Mark where platelets are.
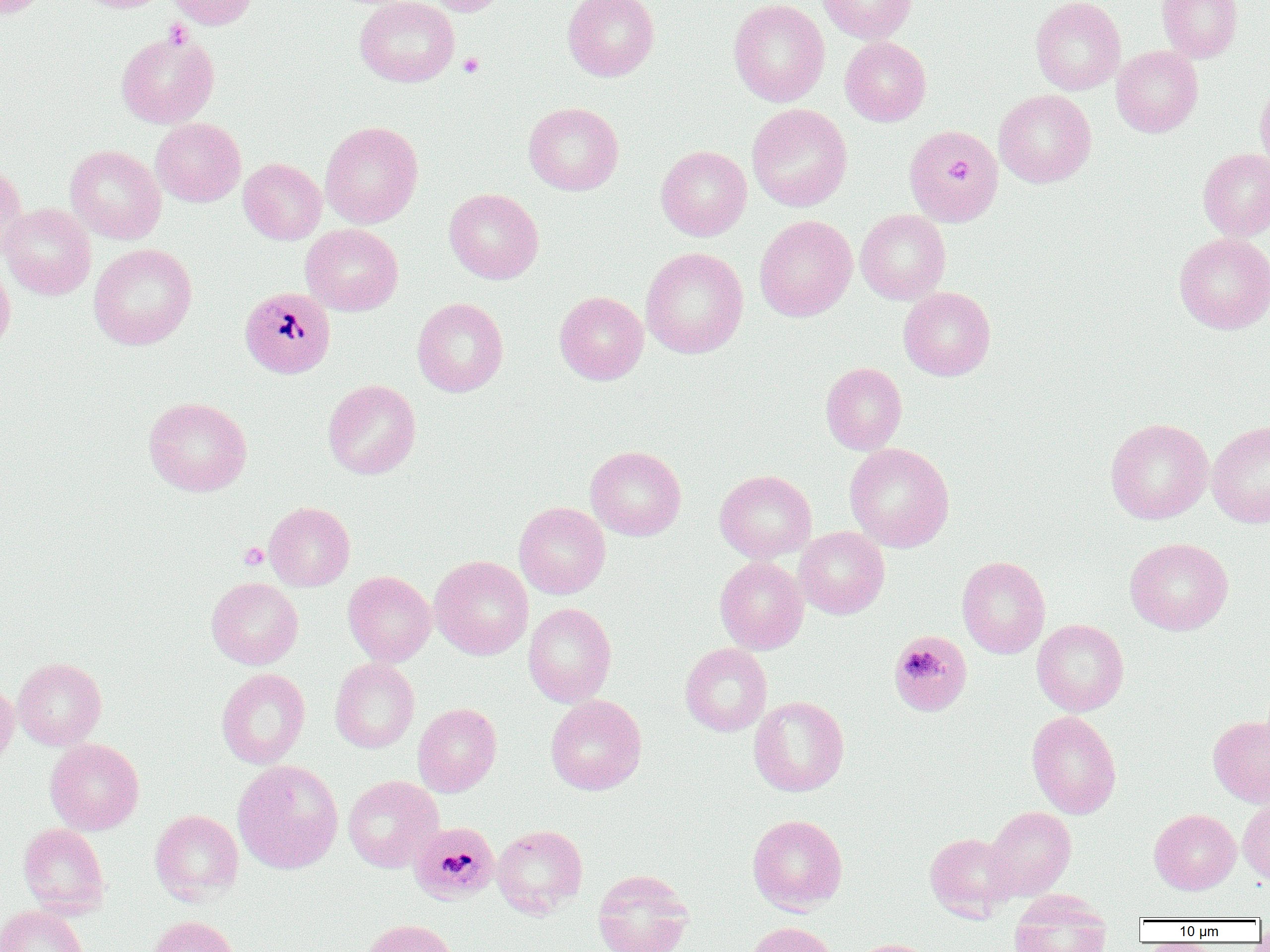

Approximate bounding boxes as named x1/y1/x2/y2 corners in pixels.
Platelets: (x1=163, y1=19, x2=193, y2=49), (x1=457, y1=53, x2=485, y2=77), (x1=239, y1=542, x2=268, y2=570).

Summary:
  - Plasmodium malariae-infected red blood cell locations: (x1=904, y1=124, x2=1003, y2=227), (x1=239, y1=286, x2=335, y2=378), (x1=890, y1=637, x2=974, y2=724), (x1=408, y1=822, x2=498, y2=904)
  - Uninfected red blood cell locations: (x1=0, y1=0, x2=52, y2=18), (x1=72, y1=0, x2=171, y2=12), (x1=166, y1=0, x2=259, y2=29), (x1=355, y1=0, x2=459, y2=86), (x1=423, y1=0, x2=510, y2=16), (x1=563, y1=0, x2=659, y2=81), (x1=729, y1=0, x2=829, y2=107), (x1=818, y1=0, x2=917, y2=43), (x1=1031, y1=0, x2=1125, y2=94), (x1=1156, y1=0, x2=1242, y2=62), (x1=116, y1=32, x2=219, y2=127), (x1=840, y1=37, x2=931, y2=126), (x1=1112, y1=46, x2=1203, y2=137), (x1=1255, y1=80, x2=1270, y2=175), (x1=994, y1=89, x2=1096, y2=188), (x1=523, y1=102, x2=624, y2=195), (x1=746, y1=103, x2=853, y2=211), (x1=151, y1=118, x2=246, y2=206), (x1=320, y1=121, x2=423, y2=228), (x1=65, y1=145, x2=166, y2=244), (x1=656, y1=145, x2=752, y2=240), (x1=1198, y1=149, x2=1270, y2=240), (x1=239, y1=158, x2=326, y2=244), (x1=0, y1=160, x2=28, y2=259), (x1=444, y1=188, x2=544, y2=284), (x1=0, y1=203, x2=96, y2=299), (x1=855, y1=209, x2=951, y2=304), (x1=755, y1=215, x2=857, y2=321), (x1=301, y1=224, x2=403, y2=316), (x1=1174, y1=232, x2=1270, y2=334), (x1=89, y1=243, x2=197, y2=349), (x1=640, y1=247, x2=748, y2=359), (x1=0, y1=260, x2=15, y2=354), (x1=898, y1=287, x2=996, y2=380), (x1=554, y1=291, x2=648, y2=384), (x1=412, y1=298, x2=508, y2=397), (x1=820, y1=362, x2=907, y2=454), (x1=323, y1=379, x2=421, y2=479), (x1=143, y1=397, x2=252, y2=496), (x1=1105, y1=418, x2=1213, y2=524), (x1=1207, y1=421, x2=1270, y2=528), (x1=844, y1=443, x2=954, y2=552), (x1=586, y1=445, x2=686, y2=541), (x1=715, y1=470, x2=817, y2=562), (x1=514, y1=501, x2=610, y2=599), (x1=264, y1=502, x2=355, y2=591), (x1=794, y1=526, x2=889, y2=618), (x1=1124, y1=537, x2=1234, y2=635), (x1=430, y1=555, x2=533, y2=660), (x1=714, y1=556, x2=809, y2=654), (x1=956, y1=556, x2=1050, y2=658), (x1=343, y1=571, x2=436, y2=666), (x1=206, y1=577, x2=303, y2=669), (x1=523, y1=603, x2=616, y2=707), (x1=1032, y1=618, x2=1129, y2=716), (x1=680, y1=643, x2=772, y2=736), (x1=12, y1=657, x2=106, y2=750), (x1=330, y1=658, x2=420, y2=753), (x1=216, y1=668, x2=311, y2=769), (x1=0, y1=680, x2=18, y2=769), (x1=545, y1=695, x2=646, y2=795), (x1=749, y1=696, x2=849, y2=796), (x1=413, y1=703, x2=502, y2=796), (x1=1026, y1=710, x2=1121, y2=819), (x1=1208, y1=715, x2=1270, y2=807), (x1=45, y1=738, x2=144, y2=835), (x1=233, y1=760, x2=343, y2=873), (x1=343, y1=775, x2=443, y2=872), (x1=1238, y1=799, x2=1270, y2=883), (x1=985, y1=806, x2=1076, y2=899), (x1=1149, y1=808, x2=1241, y2=894), (x1=150, y1=810, x2=243, y2=904), (x1=747, y1=814, x2=848, y2=913), (x1=18, y1=823, x2=109, y2=916), (x1=492, y1=824, x2=587, y2=918), (x1=925, y1=832, x2=1018, y2=921), (x1=592, y1=869, x2=694, y2=952), (x1=1008, y1=891, x2=1111, y2=952), (x1=0, y1=905, x2=88, y2=952), (x1=146, y1=915, x2=240, y2=952), (x1=361, y1=919, x2=459, y2=952), (x1=745, y1=921, x2=838, y2=952), (x1=847, y1=939, x2=938, y2=952)
  - Slide-level diagnosis: Plasmodium malariae
  - Field of view: single
  - Image size: 1270×952 pixels
  - Modality: optical microscopy
  - Preparation: thin blood smear
  - Magnification: 1000x